State which parasite is depicted.
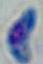

Toxoplasma gondii.

Summary:
  - Magnification: 1000x
  - Modality: micrograph